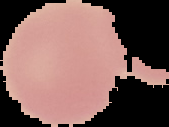 From a thin blood smear. Result: no Plasmodium parasites detected. Image is 169×127 pixels. Segmented cell region on a black background.